Point out every Plasmodium parasite and every leukocyte.
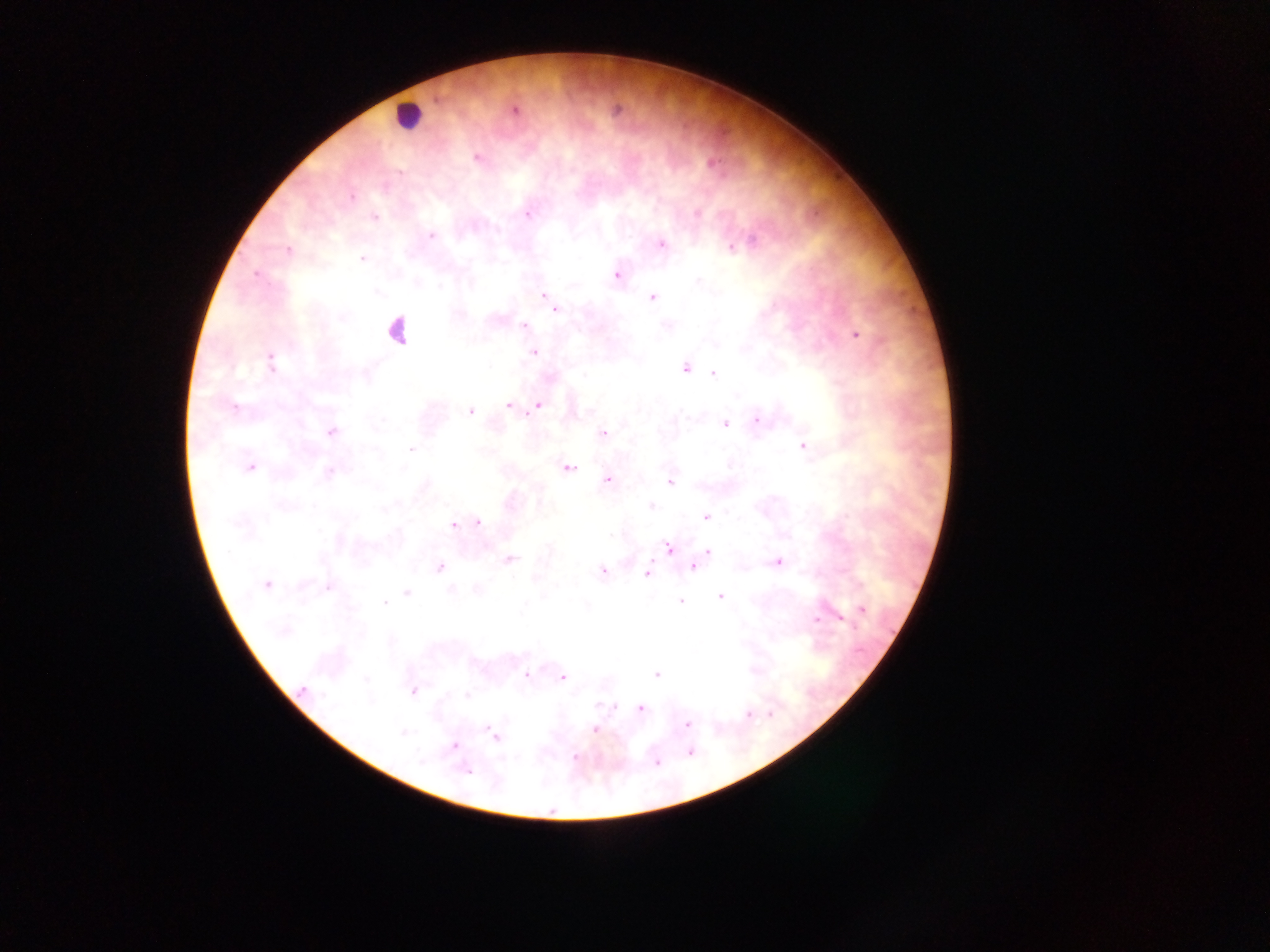

Approximate centers as (x, y) in pixels.
Plasmodium parasites: (515, 110), (617, 110), (477, 158), (712, 163), (351, 197), (528, 214), (697, 214), (374, 218), (431, 236), (751, 242), (661, 244), (732, 248), (288, 250), (362, 259), (256, 273), (617, 276), (698, 281), (543, 295), (653, 298), (555, 309), (524, 326), (856, 334), (534, 352), (270, 361), (686, 367), (713, 374), (538, 405), (233, 406), (508, 406), (469, 411), (758, 420), (725, 424), (332, 432), (604, 433), (803, 446), (411, 449), (729, 465), (250, 467), (568, 467), (329, 472), (607, 479), (670, 482), (651, 506), (706, 517), (478, 522), (453, 525), (669, 548), (708, 552), (509, 559), (778, 562), (440, 567), (693, 567), (603, 572), (647, 574), (267, 585), (329, 587), (450, 590), (407, 593), (720, 596), (681, 602), (384, 603), (863, 610), (815, 619), (840, 619), (282, 631), (656, 674), (526, 675), (563, 677), (303, 690), (414, 691), (467, 696), (602, 706), (640, 708), (748, 715), (770, 715), (687, 724), (594, 730), (403, 733), (495, 735), (454, 745), (689, 752), (576, 757), (422, 760), (657, 762), (466, 771).
Leukocytes: (406, 115), (395, 331).

Summary:
  - Field of view: single
  - Country: Ghana
  - Image size: 1270×952 pixels
  - Preparation: thick blood smear
  - Capture: mobile-phone photograph through a microscope